Report the malaria status of this cell.
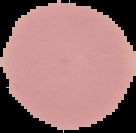
Uninfected.

preparation: thin blood film
image_size: 136×133 pixels
image_type: cell region segmented out of the field of view; surrounding area masked to black